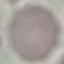

Summary:
  - Result: no malaria parasites detected
  - Capture: smartphone camera at the microscope eyepiece
  - Preparation: thin smear
  - Image type: automatically extracted cell patch, resized to 64 × 64 pixels
  - Stain: Giemsa